Locate and identify every blood parasite.
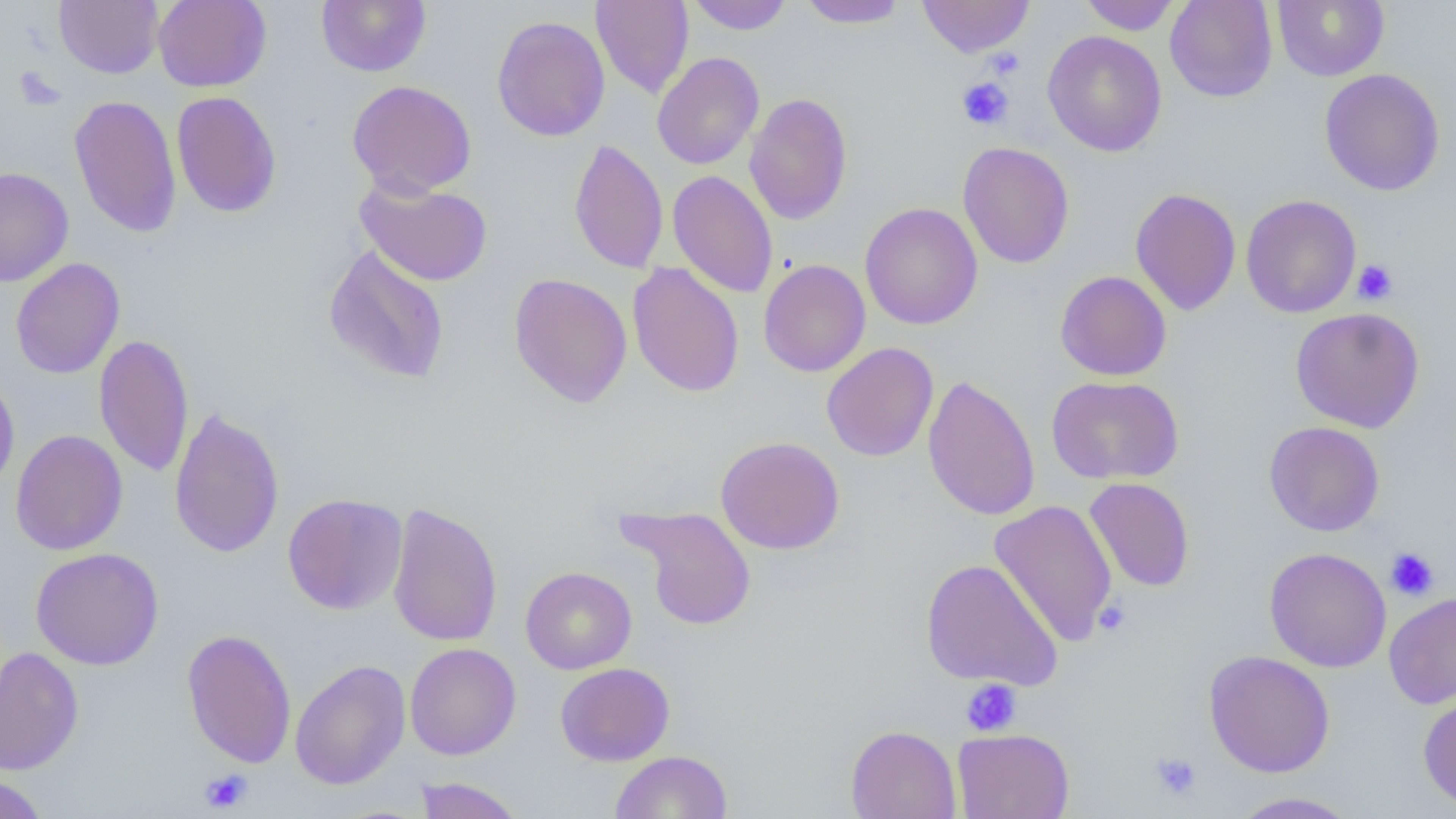

No blood parasites seen.

slide-level diagnosis = negative for blood parasites
image size = 1456×819 pixels
magnification = 1000x
preparation = thin blood smear
modality = light microscopy
field of view = single
uninfected red blood cell locations = approximate bounding boxes as (x1, y1, x2, y2) in pixels: (54, 0, 163, 78), (153, 0, 272, 92), (316, 0, 431, 76), (591, 0, 694, 99), (687, 0, 793, 35), (797, 0, 909, 29), (917, 0, 1034, 57), (1079, 0, 1181, 35), (1165, 0, 1278, 102), (1272, 0, 1389, 81), (492, 15, 610, 142), (1042, 30, 1167, 157), (652, 51, 764, 170), (1319, 68, 1445, 196), (347, 80, 477, 198), (171, 91, 282, 218), (744, 93, 853, 225), (68, 94, 182, 238), (568, 138, 669, 275), (957, 142, 1075, 269), (0, 167, 73, 286), (667, 170, 778, 298), (355, 177, 493, 287), (1130, 188, 1241, 316), (1241, 194, 1361, 318), (859, 202, 983, 330), (322, 243, 450, 385), (10, 258, 125, 379), (758, 259, 871, 377), (627, 262, 744, 398), (1054, 270, 1172, 381), (508, 272, 632, 409), (1290, 307, 1425, 433), (94, 333, 193, 478), (822, 342, 939, 461), (0, 374, 20, 493), (922, 375, 1040, 522), (1046, 375, 1184, 485), (169, 406, 284, 559), (1264, 421, 1385, 537), (11, 429, 128, 556), (715, 436, 846, 554), (1084, 477, 1195, 592), (282, 493, 407, 615), (989, 500, 1117, 646), (388, 502, 503, 648), (619, 505, 757, 631), (30, 547, 164, 670), (1264, 547, 1392, 672), (920, 558, 1063, 691), (520, 566, 637, 674), (1384, 591, 1456, 709), (182, 628, 296, 768), (405, 643, 521, 760), (0, 647, 83, 775), (1203, 650, 1335, 778), (289, 659, 410, 790), (555, 662, 675, 766), (1417, 692, 1456, 811), (845, 725, 961, 819), (952, 728, 1074, 819), (611, 750, 732, 819), (0, 774, 49, 819), (414, 777, 523, 819), (1227, 791, 1361, 818)
platelet locations = approximate bounding boxes as (x1, y1, x2, y2) in pixels: (986, 47, 1025, 80), (957, 77, 1014, 131), (1352, 259, 1399, 305), (1385, 548, 1439, 600), (1093, 599, 1132, 637), (961, 678, 1022, 738), (1150, 751, 1201, 801), (199, 768, 253, 814)